Outline each Babesia divergens-infected red blood cell.
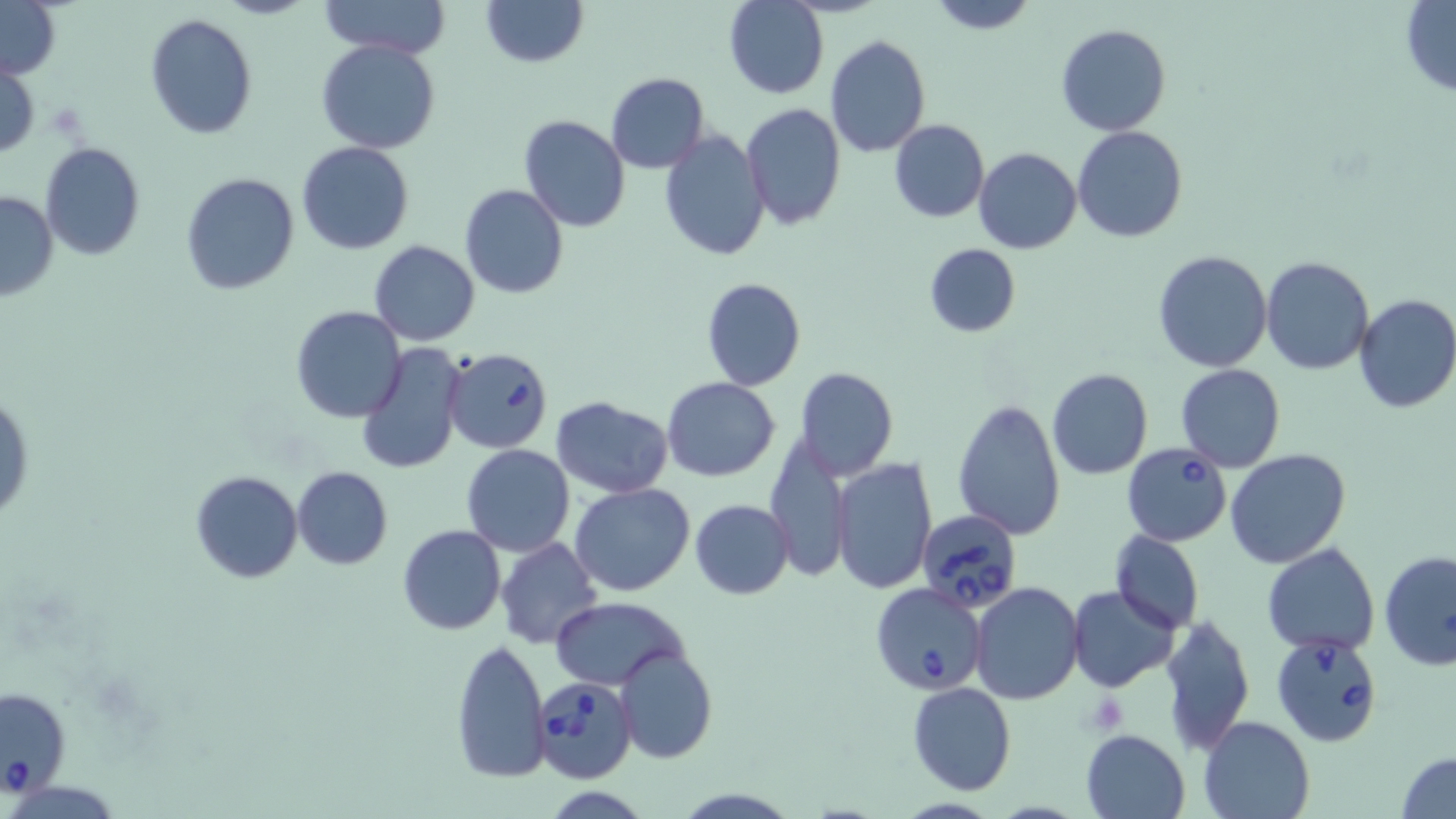
Approximate bounding boxes as (x1,y1)-(x2,y2) corner pairs in pixels.
Babesia divergens-infected red blood cells: (442,347)-(554,454), (1123,443)-(1233,546), (917,510)-(1021,613), (871,581)-(988,695), (1271,633)-(1386,749), (532,676)-(638,785), (0,683)-(71,799).

slide-level diagnosis = Babesia divergens
magnification = 1000x
field of view = single
image size = 1456×819 pixels
uninfected red blood cell locations = approximate bounding boxes as (x1,y1)-(x2,y2) corner pairs in pixels: (319,0)-(454,55), (481,0)-(586,67), (925,1)-(1039,34), (723,2)-(829,100), (1399,2)-(1456,96), (0,3)-(60,81), (144,12)-(260,140), (1055,22)-(1171,136), (825,34)-(931,157), (316,38)-(441,155), (0,63)-(39,157), (606,72)-(710,173), (740,102)-(846,229), (518,114)-(631,234), (888,119)-(989,223), (1072,126)-(1188,243), (659,129)-(772,263), (296,141)-(415,254), (39,142)-(148,261), (972,146)-(1082,254), (180,171)-(302,296), (461,185)-(568,298), (0,189)-(58,303), (368,239)-(481,347), (922,242)-(1020,338), (1153,249)-(1272,372), (1261,256)-(1373,374), (701,277)-(805,391), (1353,293)-(1456,413), (291,305)-(408,423), (357,343)-(468,476), (1176,364)-(1285,472), (794,367)-(897,481), (1046,369)-(1152,479), (664,380)-(781,483), (1,385)-(34,529), (551,397)-(673,497), (952,398)-(1066,541), (763,436)-(849,583), (461,444)-(574,557), (1227,448)-(1350,568), (833,459)-(936,595), (290,467)-(393,569), (189,469)-(303,583), (569,484)-(696,597), (690,499)-(794,599), (397,524)-(505,635), (1109,531)-(1204,633), (496,537)-(604,651), (1263,543)-(1379,655), (1379,549)-(1456,669), (970,582)-(1084,703), (1067,585)-(1179,692), (549,596)-(689,690), (1157,613)-(1255,755), (450,639)-(551,782), (613,644)-(716,765), (907,682)-(1017,795), (1198,715)-(1316,819), (1080,729)-(1190,819), (1397,750)-(1456,819)
modality = optical microscopy
stain = May-Grünwald-Giemsa
preparation = thin blood film